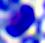

Photomicrograph. Captured at 400x magnification. A white blood cell is seen.